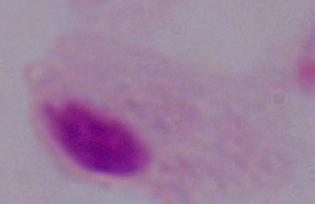

Summary:
  - Magnification: 1000x
  - Modality: photomicrograph
  - Identification: trichomonad